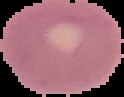
result = negative for malaria parasites
image size = 124×97 pixels
image type = segmented cell region with the area outside set to black
preparation = thin blood film